Report the malaria status of this cell.
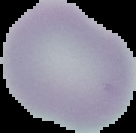

It is uninfected.

Summary:
  - Preparation: thin blood smear
  - Image type: segmented cell region with the area outside set to black
  - Image size: 136×133 pixels